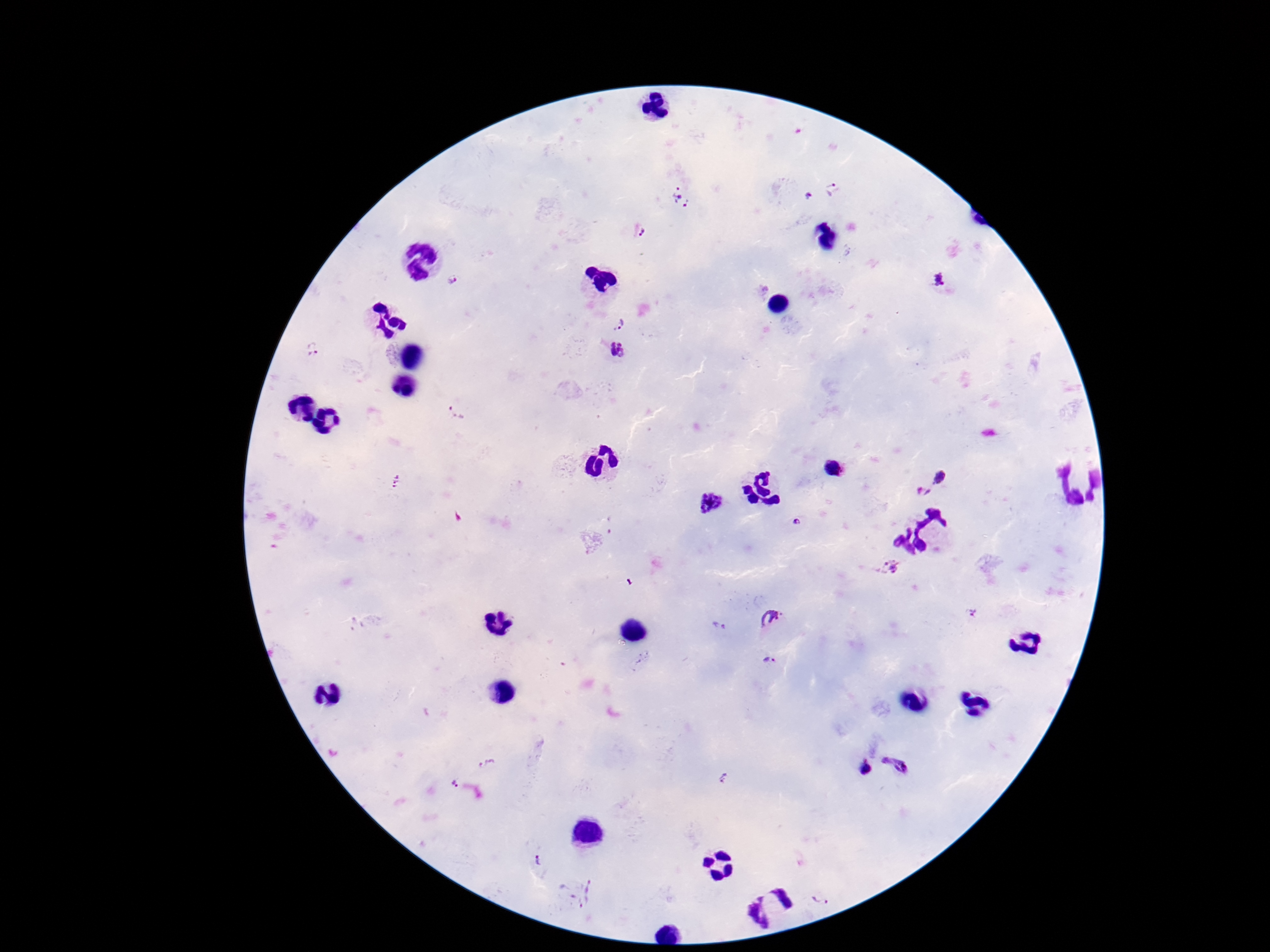
Approximate centers as (x, y) in pixels.
Summary:
  - Plasmodium parasite locations: (833, 190), (808, 196), (682, 198), (644, 234), (938, 280), (452, 281), (617, 322), (314, 348), (618, 348), (458, 412), (833, 468), (941, 473), (398, 481), (923, 492), (712, 502), (797, 522), (889, 569), (975, 611), (772, 616), (719, 627), (771, 660), (897, 763), (488, 765), (864, 768), (728, 778), (454, 785), (541, 861), (587, 894), (821, 899)
  - Field of view: single
  - Stain: Giemsa
  - Capture: smartphone camera through the microscope eyepiece
  - Magnification: 100x
  - Patient malaria status: infected
  - Image size: 1270×952 pixels
  - Preparation: thick blood smear